Give the position of every P. falciparum parasite, noting its life-cycle stage.
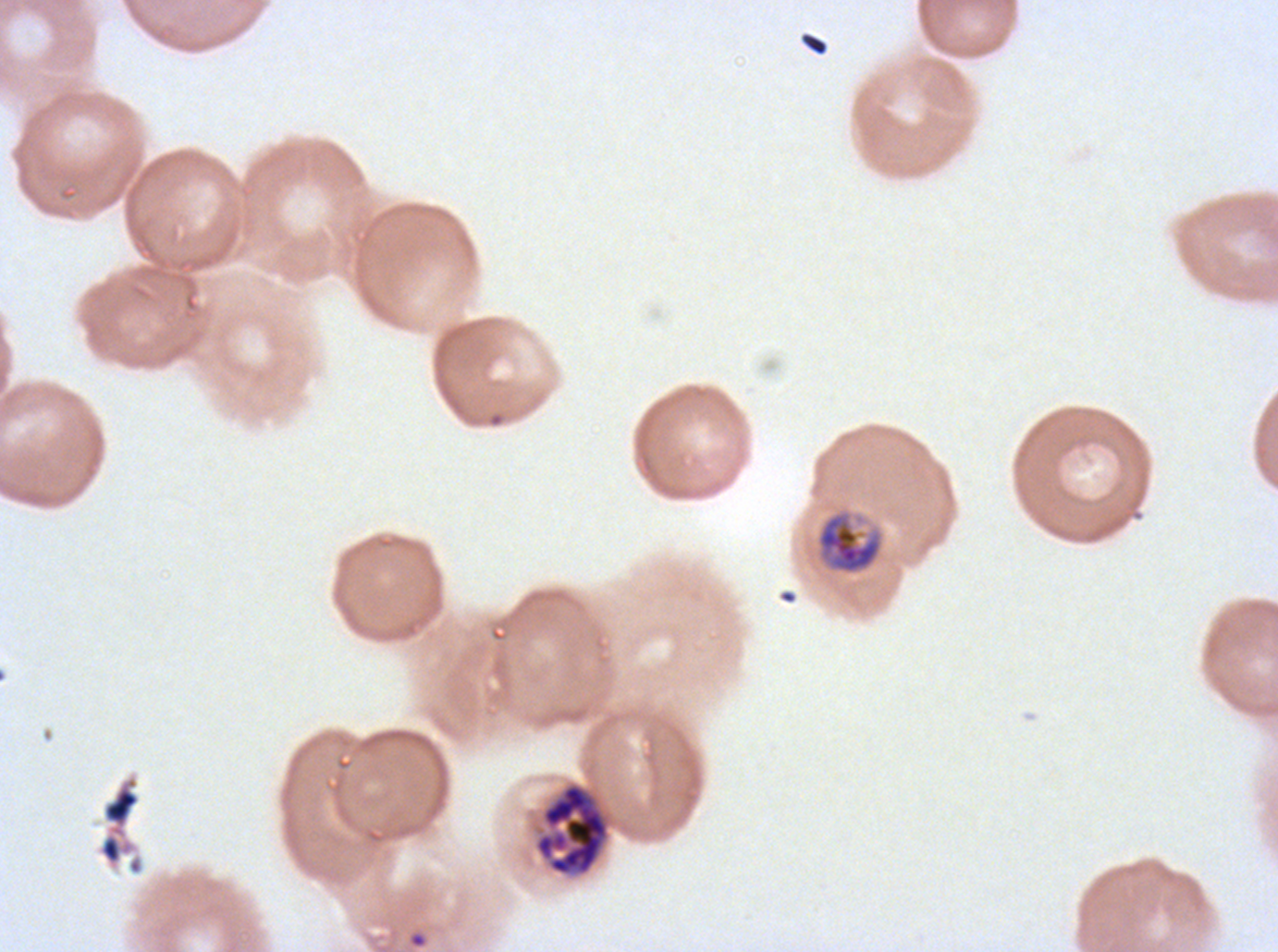

Approximate bounding boxes as (x1, y1, x2, y2) in pixels.
Rings: (409, 932, 427, 948).
Mid trophozoites: (814, 507, 885, 577).
Segmenters: (534, 782, 610, 876).
No late-ring/early-trophozoite forms, late trophozoites, early schizonts, late schizonts, or gametocytes observed.

debris locations = (801, 32, 828, 56), (96, 773, 145, 876)
specimen = ex-vivo P. falciparum culture from a patient in The Gambia, grown for 24 to 48 hours
stain = Giemsa
image size = 1278×952 pixels
field of view = one sub-image of a larger composite
life-cycle stages observed = ring, mid trophozoite, segmenter
preparation = thin blood smear